Report the malaria status of this cell.
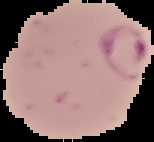
Parasitized.

image size = 154×142 pixels
image type = segmented cell region on a black background
preparation = thin blood film